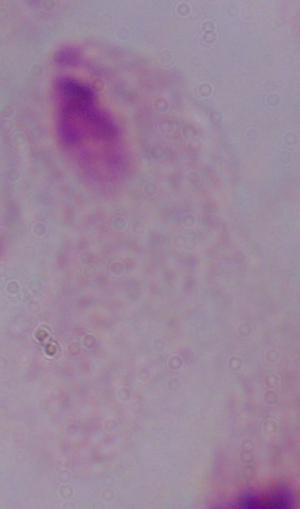

modality = photomicrograph
identification = trichomonad
magnification = 1000x